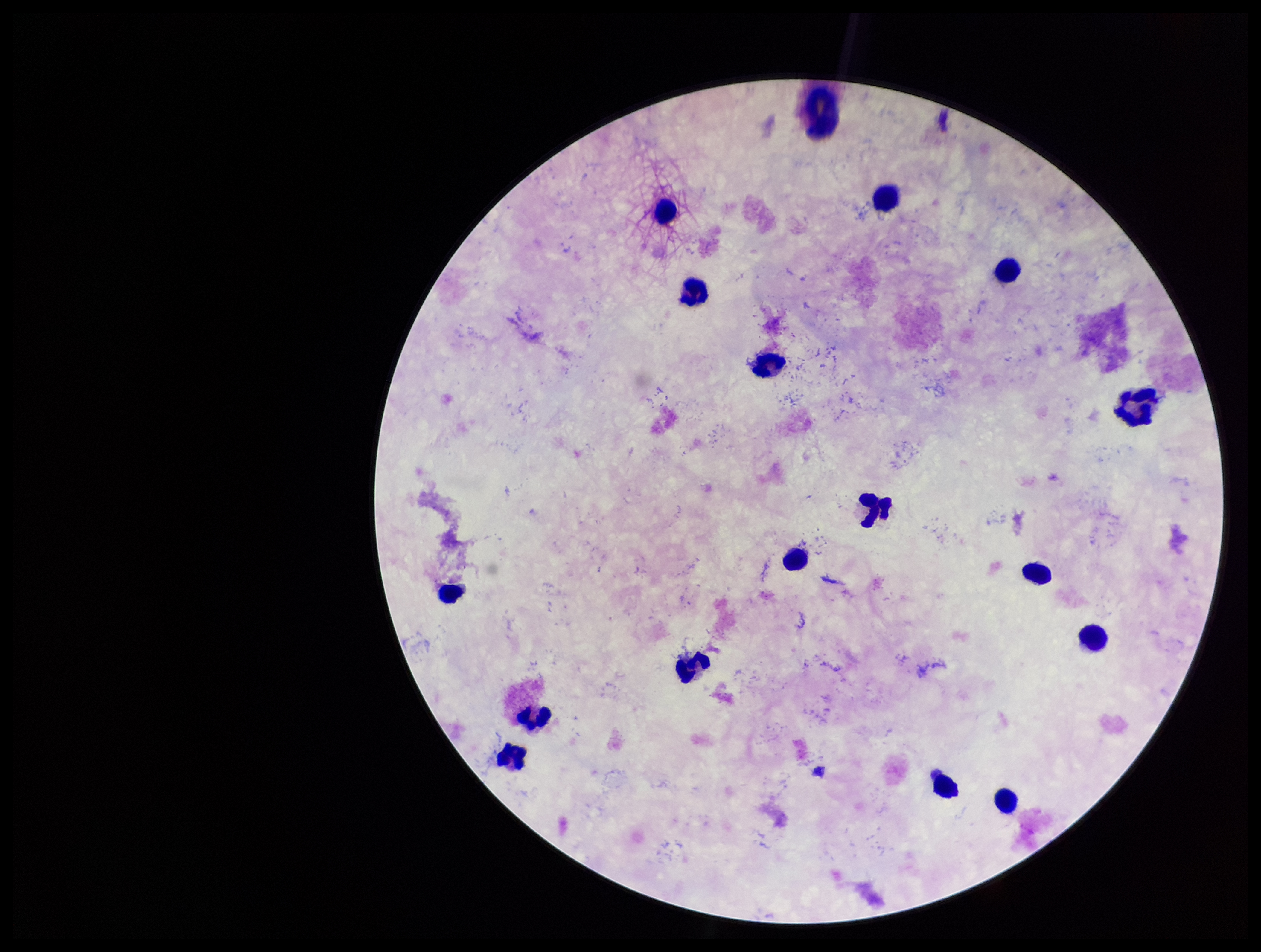

Leukocyte count: 16. Image is 1261×952 pixels. Photographed through the microscope eyepiece with a smartphone camera. Patient malaria status: negative. Stained with Giemsa. Plasmodium parasites: none seen. Preparation: thick. Single field of view. Parasite count: 0.